Assess the morphology of the erythrocytes.
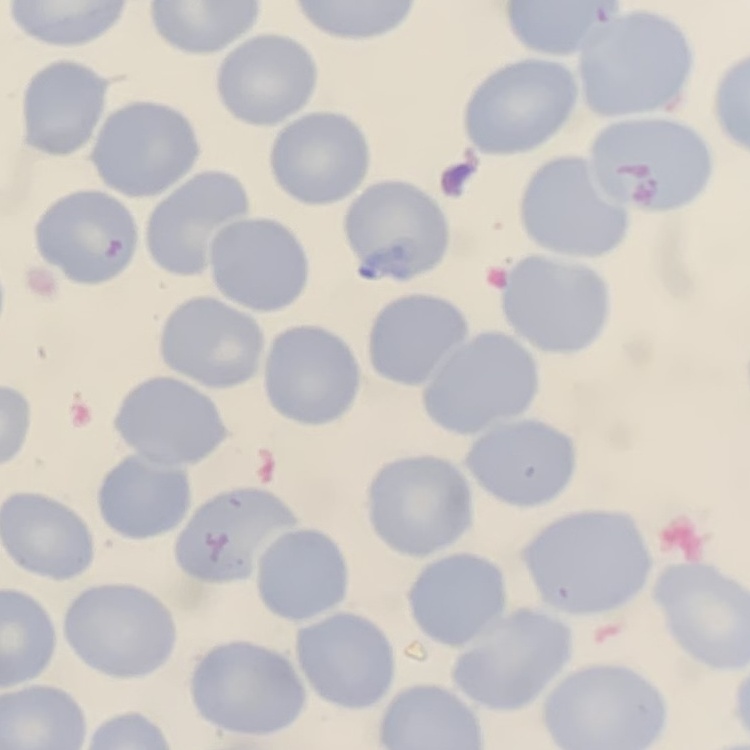
They show no rouleaux formation.

Field's or Giemsa stain. Thin peripheral smear. One tile cut from a larger photomicrograph.